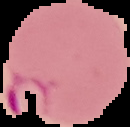
From a thin blood film. Image is 130×127 pixels. Result: Plasmodium parasites identified. Segmented cell region on a black background.